Give a bounding box for every leukocyte visible.
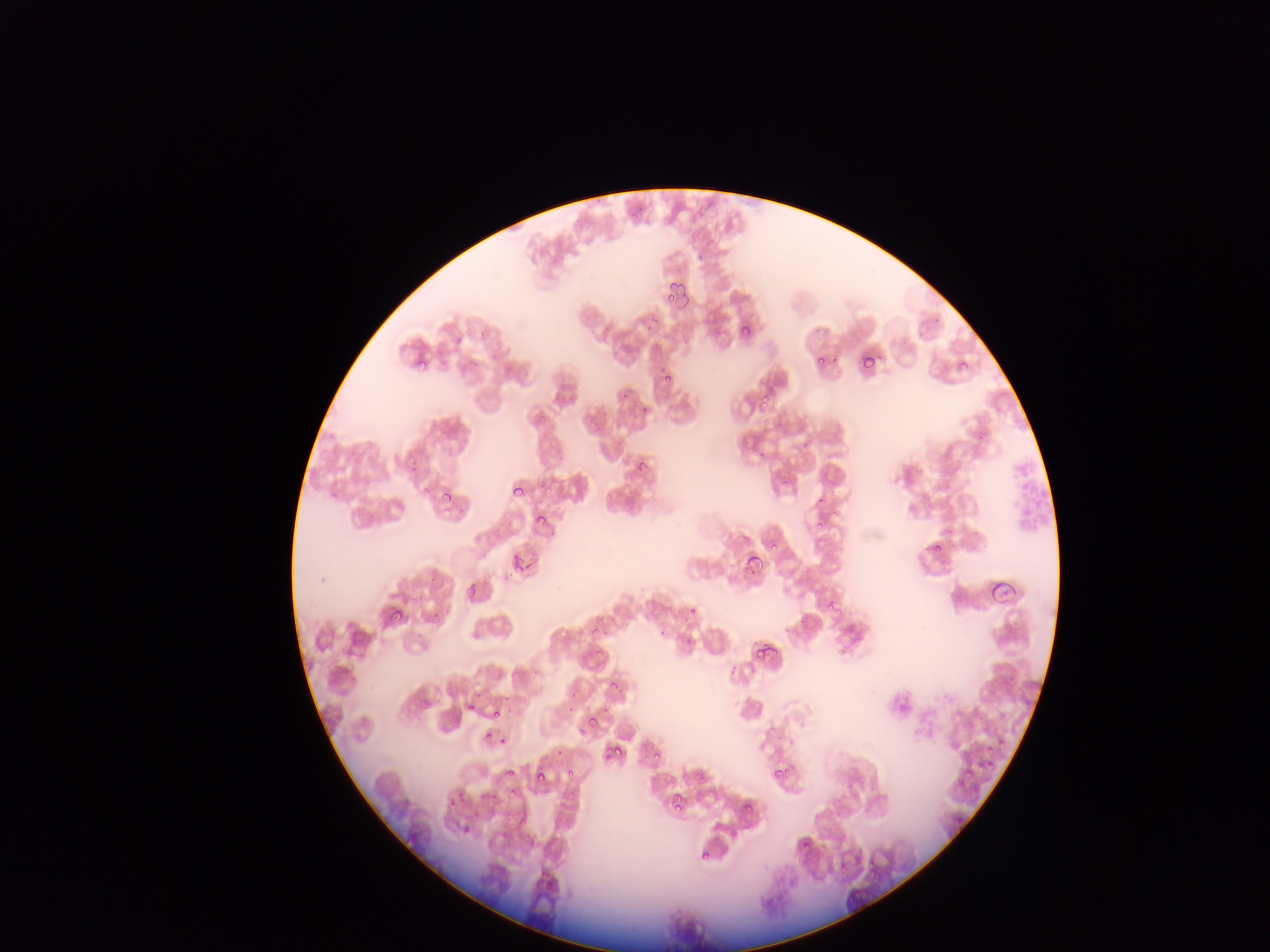

No leukocytes observed.

Approximate bounding boxes as (left, top, right, bottom) in pixels. Plasmodium parasite locations: (595, 198, 605, 204), (637, 205, 645, 212), (574, 217, 579, 225), (698, 254, 705, 262), (676, 280, 687, 295), (670, 282, 678, 291), (676, 293, 689, 309), (667, 295, 675, 302), (651, 315, 658, 323), (742, 326, 751, 337), (861, 352, 874, 371), (878, 352, 883, 361), (491, 354, 500, 358), (816, 354, 825, 365), (829, 355, 840, 364), (417, 357, 427, 369), (959, 360, 968, 368), (663, 377, 673, 386), (762, 394, 771, 403), (781, 480, 789, 486), (422, 485, 430, 493), (510, 486, 527, 500), (440, 494, 453, 503), (818, 496, 826, 505), (537, 516, 546, 524), (815, 522, 823, 530), (933, 541, 944, 550), (770, 543, 778, 548), (512, 554, 521, 564), (748, 555, 763, 571), (525, 564, 533, 571), (514, 566, 523, 571), (989, 579, 1017, 606), (464, 584, 477, 598), (690, 606, 697, 614), (388, 607, 404, 623), (835, 607, 843, 615), (658, 629, 667, 636), (593, 631, 601, 636), (766, 645, 779, 659), (756, 649, 764, 659), (730, 665, 737, 677), (1009, 675, 1017, 682), (608, 681, 619, 692), (504, 695, 512, 702), (467, 705, 475, 712), (493, 711, 501, 718), (587, 720, 596, 727), (579, 725, 584, 735), (997, 741, 1005, 746), (615, 747, 623, 758), (555, 750, 563, 754), (654, 751, 660, 759), (605, 752, 611, 761), (784, 765, 792, 776), (508, 767, 514, 776), (773, 768, 782, 779), (564, 769, 576, 777), (964, 769, 972, 778), (535, 775, 543, 783), (459, 789, 466, 798), (672, 795, 681, 801), (449, 799, 456, 809), (674, 801, 685, 811), (744, 802, 752, 813), (474, 810, 480, 819), (956, 812, 964, 823), (462, 824, 472, 836), (700, 851, 710, 862), (867, 860, 875, 867) | approximate (x, y) pixel centers of objects too small to bound: (634, 216), (937, 320), (649, 329), (921, 335), (458, 341), (664, 370), (624, 396), (764, 405), (644, 411), (980, 435), (807, 445), (762, 454), (414, 462), (642, 463), (413, 468), (549, 489), (334, 496), (446, 510), (950, 531), (976, 533), (510, 576), (432, 580), (830, 601), (830, 608), (436, 616), (1015, 624), (606, 633), (689, 640), (599, 652), (574, 695), (572, 708), (606, 711), (489, 735), (502, 741), (991, 748), (647, 756), (991, 763), (980, 764), (540, 768), (513, 792), (495, 796), (807, 846), (873, 872). Single field of view. Image is 1270×952 pixels. Thin blood film. Mobile-phone photograph taken through the microscope. Collected in Ghana.